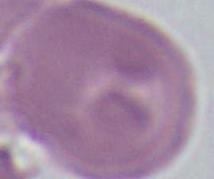 An erythrocyte is shown. Micrograph. Captured at 1000x magnification.